Report the malaria status of this cell.
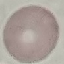
Uninfected.

Acquired by smartphone through the microscope eyepiece. Thin blood film. Cell patch, automatically extracted from a larger field of view and resized to 64 × 64 pixels. Giemsa-stained preparation.